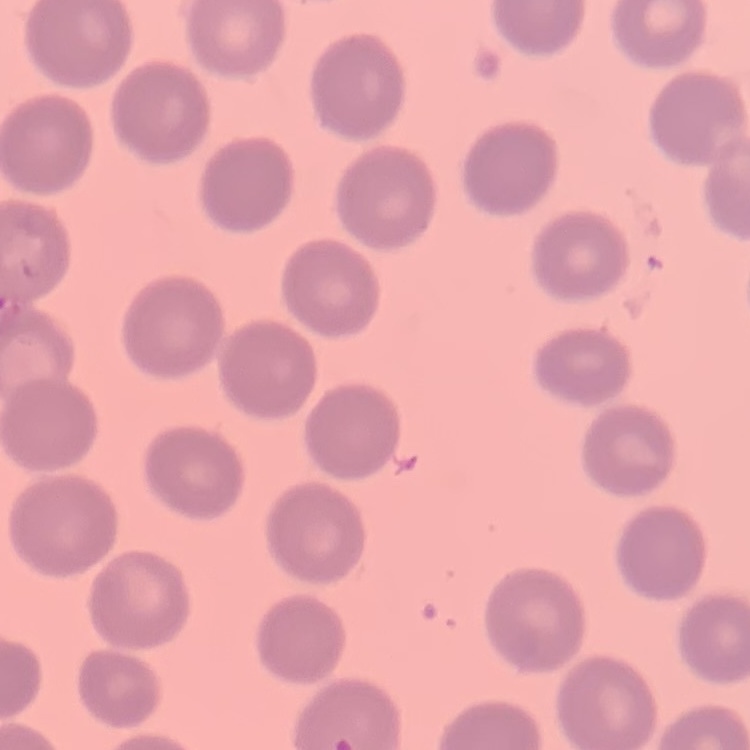
red blood cell morphology = no rouleaux formation
image type = one tile cut from a larger photomicrograph
preparation = thin blood film
stain = Field's or Giemsa